Locate every Plasmodium parasite.
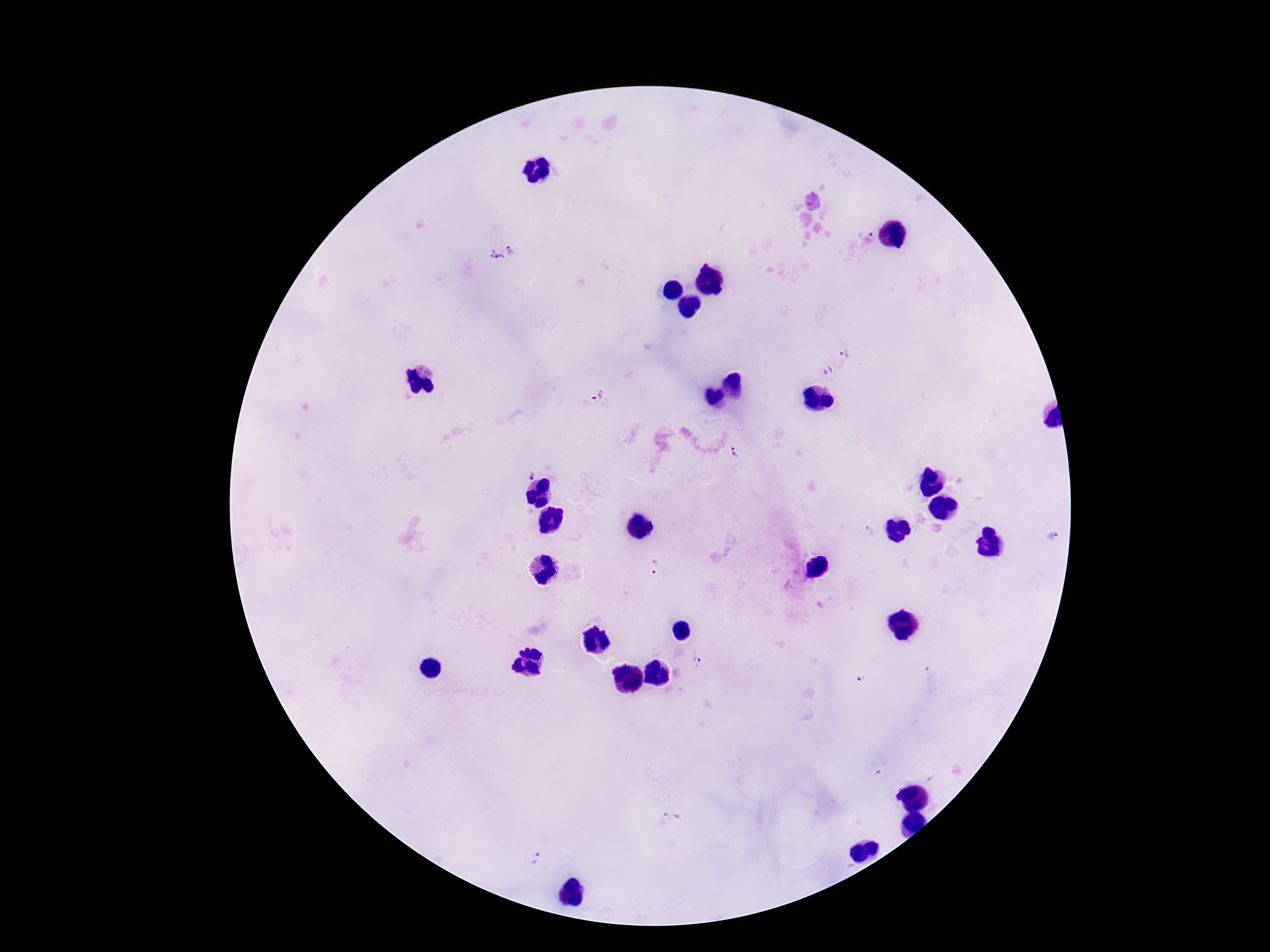
Approximate centers as {x, y} in pixels.
Plasmodium parasites: {511, 250}, {497, 256}, {847, 351}, {828, 371}, {598, 395}, {735, 453}, {526, 470}, {869, 530}, {1053, 536}, {656, 568}, {699, 658}, {861, 677}, {674, 814}, {536, 858}.

preparation = thick blood smear
image size = 1270×952 pixels
capture = smartphone camera through the microscope eyepiece
field of view = single
magnification = 100x
stain = Giemsa
patient malaria status = positive